Assess this cell for malaria.
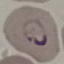

Parasitized.

Summary:
  - Preparation: thin blood film
  - Stain: Giemsa
  - Image type: cell patch, automatically extracted from a larger field of view and resized to 64 × 64 pixels
  - Capture: smartphone camera at the microscope eyepiece